Identify the parasite.
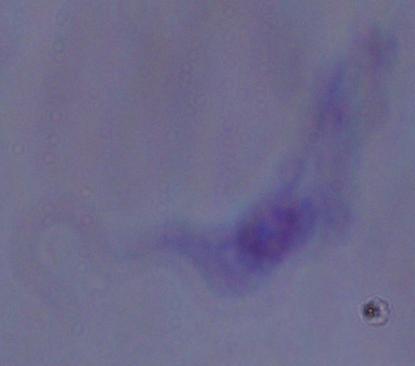
This is a trypanosome.

magnification = 1000x
modality = photomicrograph